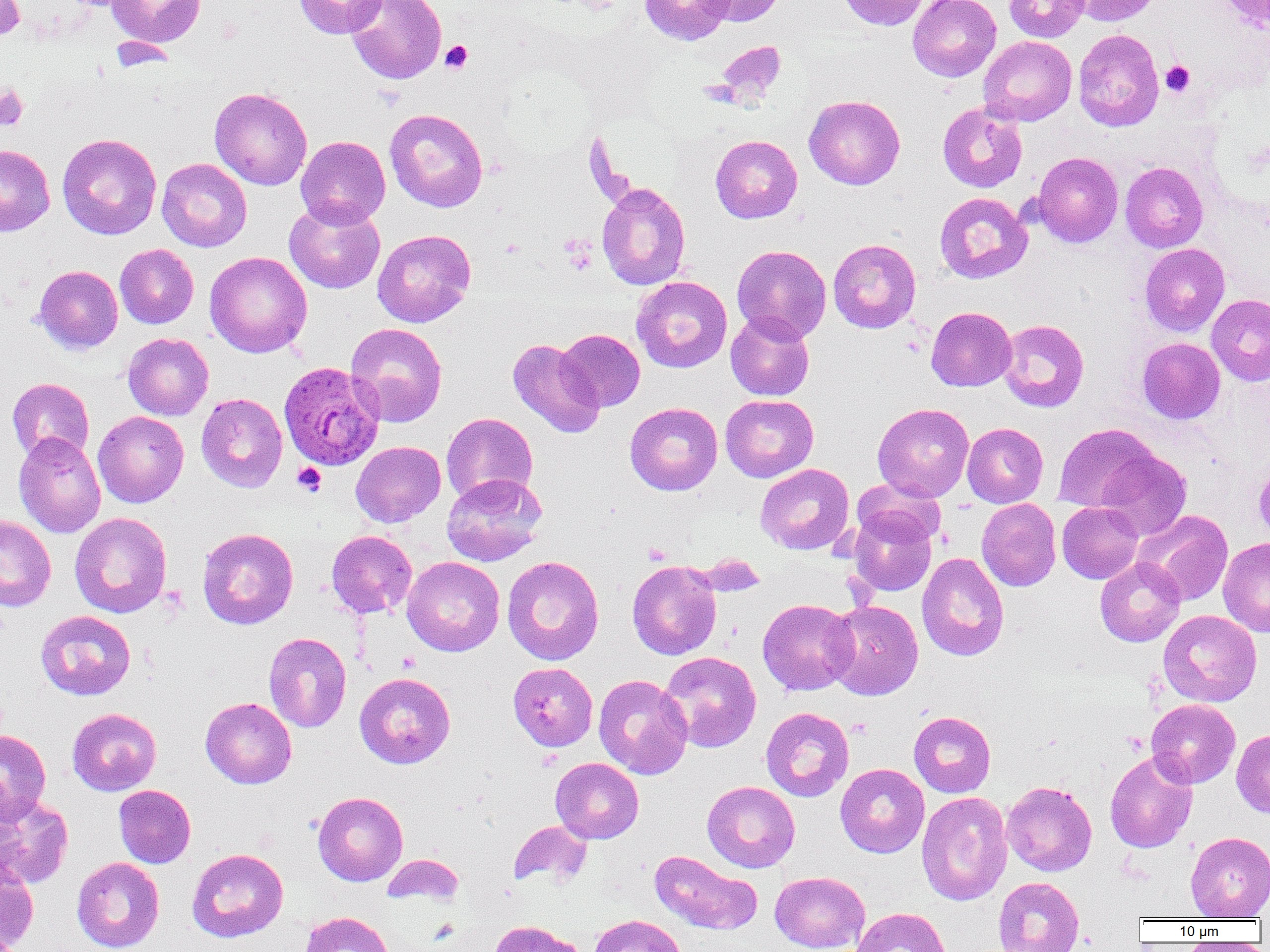

slide-level diagnosis = Plasmodium ovale
magnification = 1000x
image size = 1270×952 pixels
preparation = thin blood film
Plasmodium ovale-infected red blood cell locations = approximate bounding boxes as (x1, y1, x2, y2) in pixels: (278, 361, 384, 470)
field of view = one of a larger specimen
uninfected red blood cell locations = approximate bounding boxes as (x1, y1, x2, y2) in pixels: (0, 0, 25, 41), (106, 0, 205, 47), (294, 0, 387, 38), (345, 0, 446, 84), (639, 0, 734, 45), (697, 0, 788, 26), (837, 0, 931, 30), (908, 0, 1001, 81), (1004, 0, 1090, 42), (1071, 0, 1162, 26), (1216, 0, 1270, 32), (1073, 29, 1164, 131), (979, 36, 1077, 126), (713, 40, 787, 106), (210, 87, 312, 190), (804, 95, 905, 189), (937, 102, 1027, 193), (385, 108, 488, 212), (57, 133, 161, 240), (295, 135, 390, 228), (710, 135, 802, 223), (0, 144, 55, 236), (1033, 152, 1123, 246), (157, 158, 251, 251), (1120, 162, 1207, 252), (597, 181, 690, 290), (934, 192, 1032, 283), (284, 199, 385, 294), (372, 229, 476, 327), (828, 239, 921, 333), (1140, 243, 1230, 336), (115, 244, 198, 328), (731, 245, 832, 343), (205, 251, 312, 357), (35, 265, 123, 354), (631, 276, 732, 372), (1206, 294, 1270, 386), (926, 306, 1017, 391), (726, 311, 815, 401), (998, 319, 1089, 412), (346, 323, 447, 427), (556, 329, 645, 411), (123, 332, 214, 420), (1137, 337, 1225, 424), (507, 338, 605, 438), (7, 378, 94, 463), (196, 393, 287, 492), (720, 394, 818, 482), (625, 402, 723, 495), (872, 403, 974, 501), (93, 411, 188, 507), (441, 412, 537, 505), (962, 423, 1048, 508), (1053, 423, 1159, 513), (13, 432, 105, 538), (351, 441, 446, 527), (1097, 450, 1191, 541), (755, 463, 854, 555), (1253, 463, 1270, 541), (441, 473, 547, 566), (852, 479, 946, 547), (976, 498, 1061, 591), (1057, 502, 1143, 583), (848, 510, 936, 597), (1133, 510, 1233, 606), (70, 512, 172, 618), (0, 515, 56, 611), (197, 527, 298, 629), (326, 530, 417, 618), (1218, 537, 1270, 636), (916, 552, 1009, 661), (502, 555, 604, 665), (402, 556, 505, 656), (1095, 557, 1185, 647), (627, 560, 722, 660), (757, 598, 858, 695), (824, 600, 924, 700), (35, 610, 136, 700), (1158, 610, 1262, 707), (263, 632, 351, 732), (659, 651, 761, 752), (508, 662, 597, 751), (355, 672, 455, 769), (593, 674, 693, 779), (200, 697, 297, 788), (1146, 699, 1240, 788), (67, 707, 162, 796), (761, 707, 854, 802), (909, 711, 996, 797), (0, 729, 51, 824), (1231, 729, 1270, 818), (1105, 751, 1198, 853), (550, 757, 643, 844), (835, 763, 929, 858), (702, 781, 800, 873), (1002, 781, 1097, 876), (113, 785, 196, 868), (313, 791, 408, 886), (916, 791, 1012, 906), (0, 795, 74, 889), (509, 820, 592, 888), (1185, 831, 1270, 920), (187, 848, 288, 942), (649, 850, 762, 935), (382, 853, 465, 905), (71, 857, 164, 952), (0, 858, 39, 951), (770, 871, 870, 952), (993, 876, 1084, 952), (851, 907, 950, 952), (300, 911, 394, 952), (589, 914, 688, 952), (489, 920, 584, 952)
modality = light microscopy
platelet locations = approximate bounding boxes as (x1, y1, x2, y2) in pixels: (440, 40, 473, 73), (1161, 61, 1195, 96), (0, 85, 29, 131), (561, 236, 597, 274), (292, 462, 326, 496), (643, 543, 671, 564), (398, 651, 420, 672), (849, 718, 872, 738)